Report the malaria status of this cell.
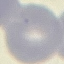
It is uninfected.

Photographed with a smartphone camera at the microscope eyepiece. Giemsa-stained preparation. Thin smear of blood. Cell patch, automatically extracted from a larger field of view and resized to 64 × 64 pixels.